Locate every leukocyte (white blood cell).
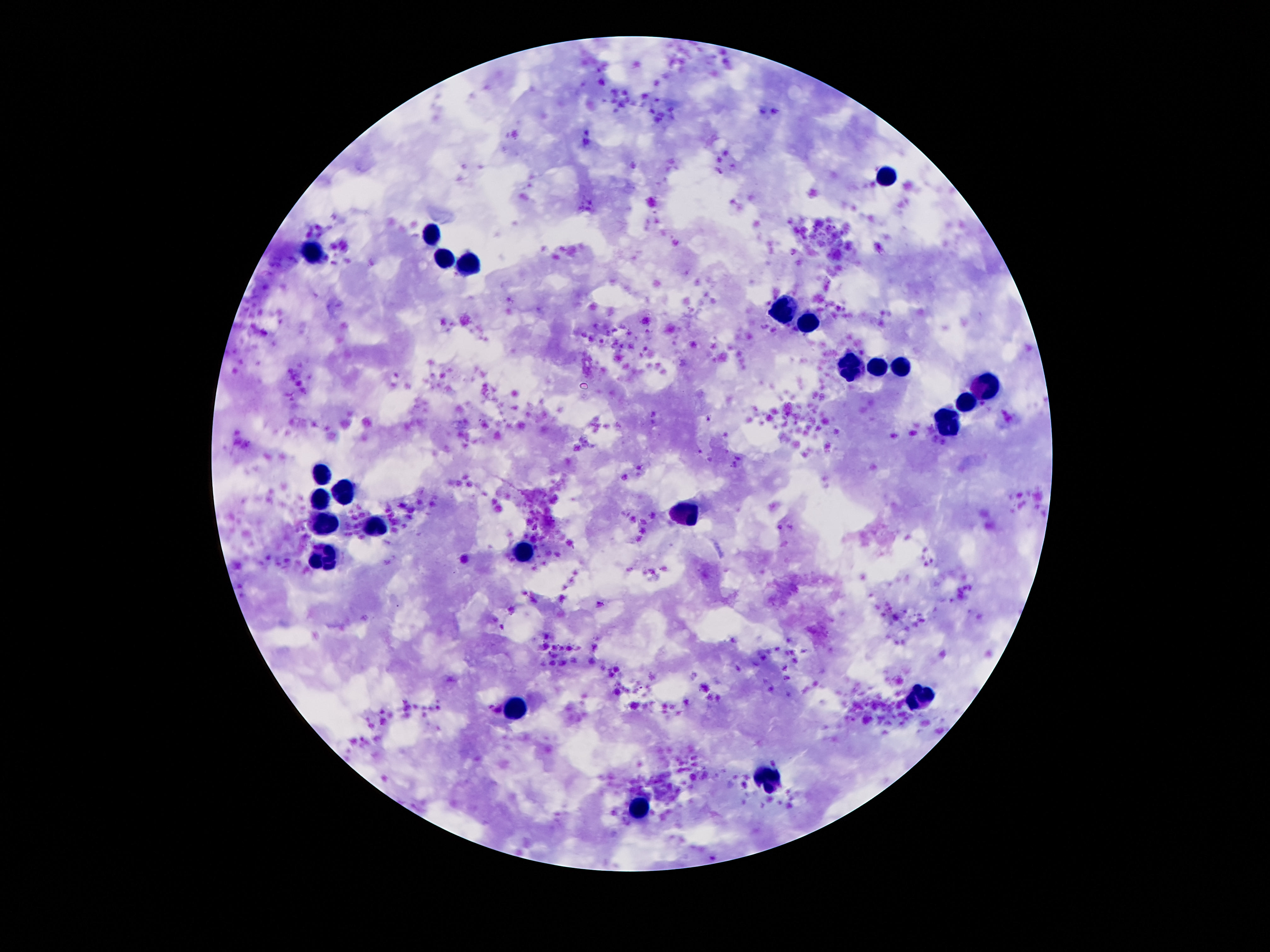
Approximate object centers, in pixels from the top-left corner.
Leukocytes: (x=885, y=175), (x=434, y=233), (x=314, y=251), (x=445, y=259), (x=469, y=264), (x=784, y=310), (x=810, y=321), (x=901, y=366), (x=877, y=368), (x=851, y=369), (x=983, y=390), (x=967, y=402), (x=949, y=422), (x=323, y=473), (x=347, y=491), (x=323, y=497), (x=690, y=511), (x=326, y=521), (x=378, y=528), (x=325, y=554), (x=523, y=555), (x=919, y=697), (x=510, y=711), (x=770, y=779), (x=643, y=809).

Summary:
  - Capture: smartphone camera through the microscope eyepiece
  - Preparation: thick peripheral-blood smear
  - Stain: Giemsa
  - Image size: 1270×952 pixels
  - Patient malaria status: not infected
  - Magnification: 100x
  - Field of view: one from this slide